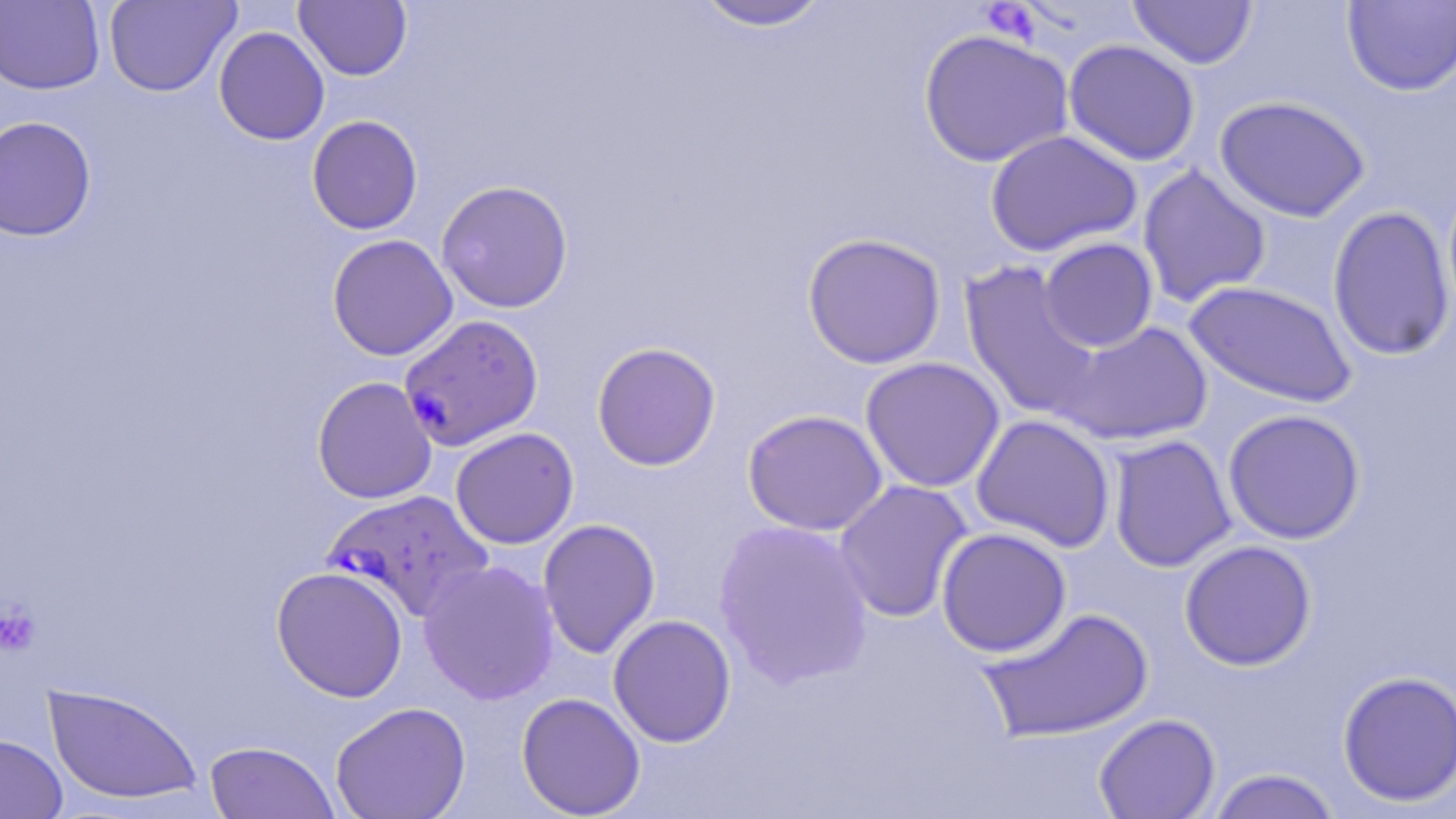
Summary:
  - Coordinate format: approximate bounding boxes as (x1,y1)-(x2,y2) corner pairs in pixels
  - Plasmodium falciparum-infected red blood cell locations: (398,313)-(543,450), (322,489)-(494,623)
  - Uninfected red blood cell locations: (104,0)-(240,97), (294,0)-(412,81), (1126,0)-(1259,69), (0,1)-(105,95), (690,1)-(836,32), (1341,1)-(1456,96), (213,26)-(330,145), (918,29)-(1074,168), (1063,39)-(1201,166), (1214,95)-(1371,222), (0,115)-(97,241), (307,115)-(423,235), (984,129)-(1142,257), (1136,165)-(1272,309), (436,180)-(574,313), (1327,205)-(1455,361), (802,232)-(946,369), (327,234)-(458,360), (1038,237)-(1159,353), (960,261)-(1104,423), (1183,280)-(1357,409), (1055,319)-(1213,446), (592,341)-(721,471), (860,356)-(1006,493), (312,376)-(437,504), (1222,408)-(1366,544), (742,409)-(889,536), (970,414)-(1116,552), (450,427)-(579,549), (1108,434)-(1236,573), (833,479)-(974,623), (537,518)-(660,659), (714,519)-(875,689), (936,527)-(1072,657), (1179,540)-(1317,670), (417,559)-(560,705), (271,566)-(409,702), (975,604)-(1155,744), (607,614)-(736,747), (1336,670)-(1456,807), (43,683)-(203,805), (516,692)-(646,818), (330,701)-(471,819), (1093,713)-(1221,819), (0,733)-(68,818), (204,741)-(339,819), (1205,768)-(1343,819)
  - Platelet locations: (981,2)-(1041,44), (0,602)-(40,656)
  - Slide-level diagnosis: Plasmodium falciparum
  - Preparation: thin blood film
  - Stain: May-Grünwald-Giemsa
  - Modality: optical microscopy
  - Magnification: 1000x
  - Image size: 1456×819 pixels
  - Field of view: one of a larger specimen